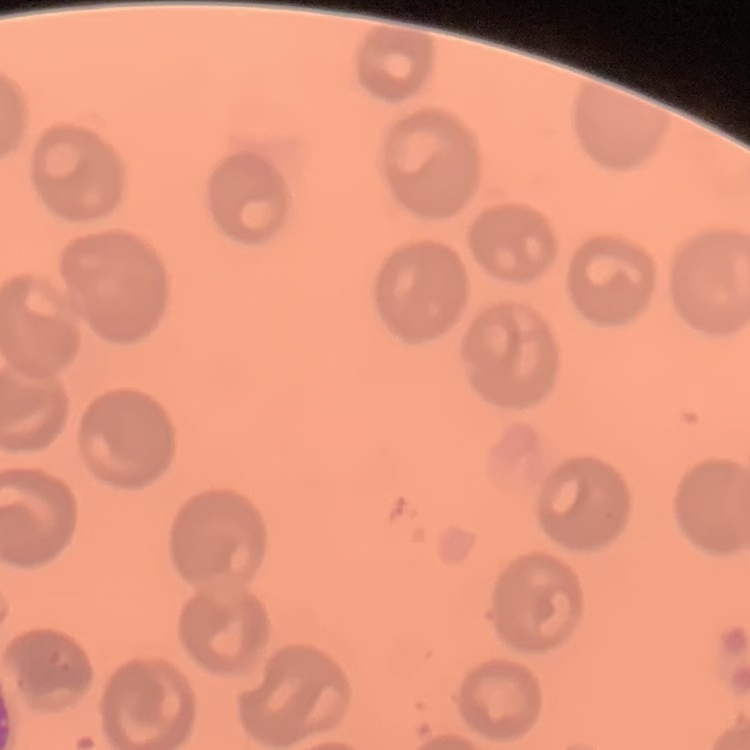
The red blood cells show no rouleaux formation. One tile cut from a larger photomicrograph. Thin blood smear. Stained with either Field's or Giemsa.